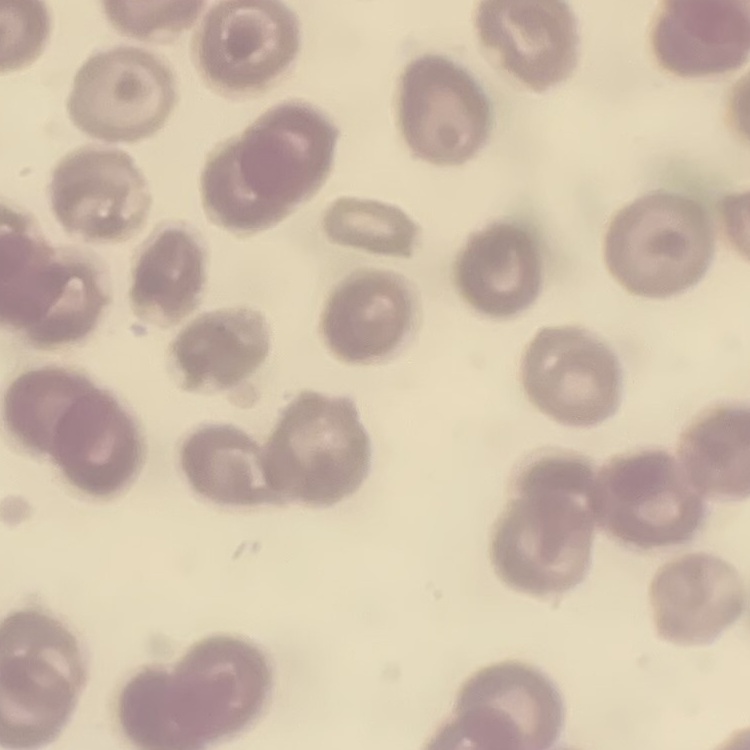

The red blood cells show no rouleaux formation. Field's or Giemsa stain. Square crop of a larger photomicrograph. Thin peripheral smear.